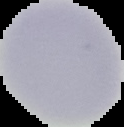 From a thin blood smear. Segmented cell region on a black background. Image is 124×127 pixels. Malaria status: uninfected.